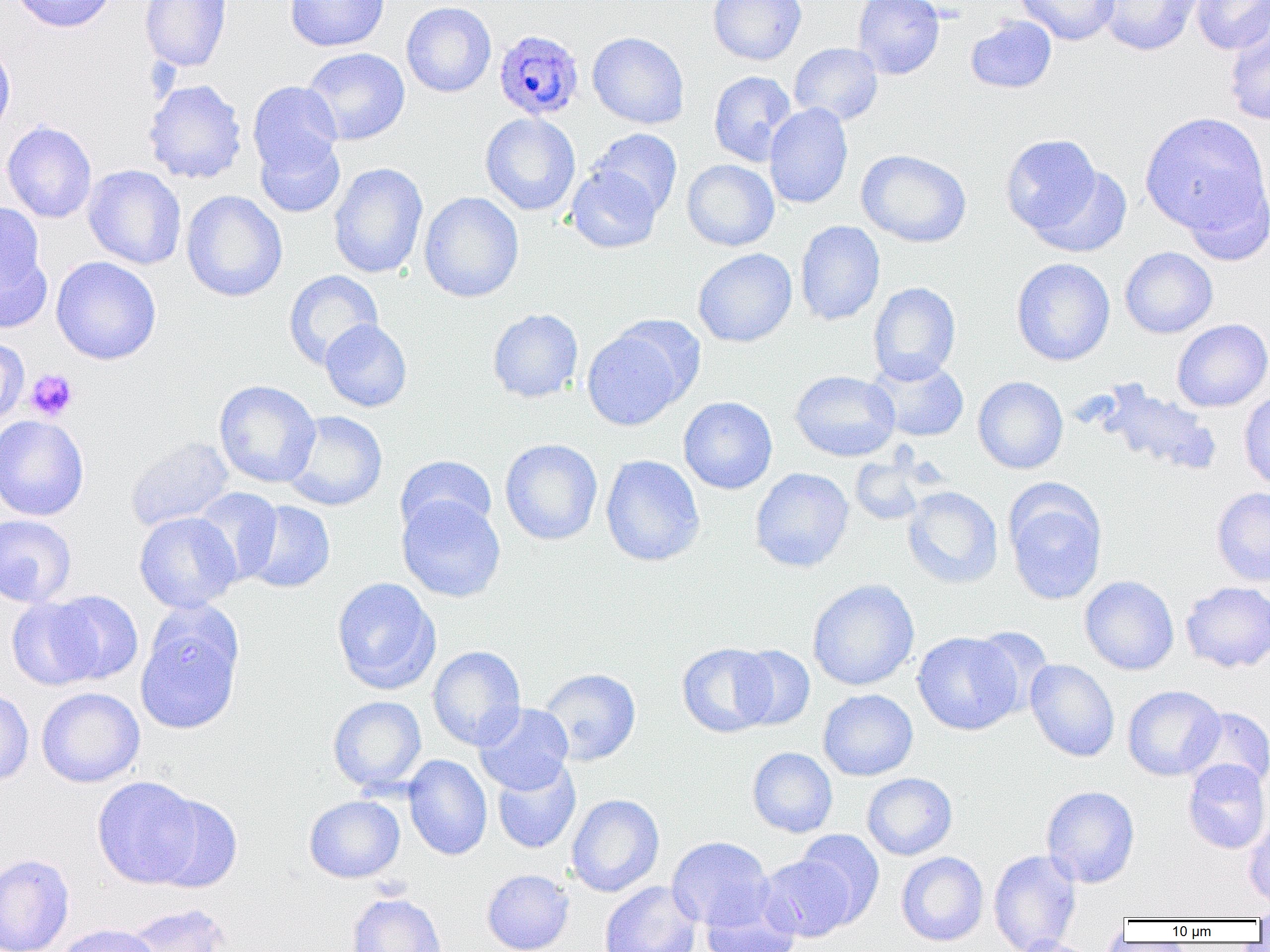
Summary:
  - Coordinate format: approximate bounding boxes as (x1, y1, x2, y2) in pixels
  - Platelet locations: (25, 369, 78, 422)
  - Uninfected red blood cell locations: (9, 0, 117, 33), (140, 0, 232, 71), (284, 0, 390, 52), (707, 0, 807, 65), (852, 0, 945, 79), (1016, 0, 1121, 45), (1097, 0, 1204, 56), (1191, 0, 1269, 55), (401, 1, 497, 97), (966, 15, 1057, 94), (1223, 16, 1270, 126), (587, 32, 689, 129), (0, 37, 15, 142), (788, 42, 883, 126), (302, 47, 410, 145), (708, 70, 798, 166), (143, 79, 248, 184), (248, 81, 343, 175), (764, 103, 853, 209), (480, 112, 581, 216), (1140, 113, 1268, 235), (2, 121, 97, 223), (589, 128, 683, 217), (254, 133, 346, 218), (999, 134, 1107, 239), (856, 149, 972, 248), (682, 159, 779, 251), (328, 162, 428, 279), (1027, 163, 1133, 257), (83, 164, 186, 270), (566, 165, 662, 253), (1180, 170, 1269, 265), (181, 190, 287, 302), (419, 191, 524, 302), (0, 202, 51, 325), (795, 220, 885, 326), (1120, 247, 1218, 338), (693, 248, 797, 347), (1012, 254, 1217, 348), (50, 256, 162, 365), (1011, 257, 1115, 366), (283, 270, 383, 370), (868, 281, 961, 384), (487, 308, 584, 402), (320, 319, 412, 412), (1172, 319, 1270, 412), (581, 323, 696, 431), (0, 337, 29, 427), (867, 357, 969, 442), (789, 370, 900, 462), (972, 376, 1068, 474), (214, 380, 320, 488), (1091, 380, 1222, 477), (1239, 389, 1270, 492), (678, 396, 777, 494), (283, 410, 388, 511), (0, 415, 89, 521), (125, 436, 234, 532), (500, 438, 603, 545), (600, 454, 705, 566), (850, 454, 930, 526), (395, 455, 497, 539), (749, 467, 854, 572), (1005, 484, 1107, 605), (903, 486, 1003, 589), (191, 487, 283, 585), (1211, 487, 1270, 587), (397, 495, 506, 602), (242, 500, 335, 593), (134, 511, 241, 614), (0, 514, 77, 607), (1079, 575, 1179, 675), (331, 577, 440, 695), (808, 579, 919, 691), (1180, 581, 1270, 672), (45, 590, 143, 685), (7, 596, 103, 691), (136, 612, 242, 735), (969, 626, 1051, 717), (912, 631, 1022, 735), (677, 642, 777, 738), (988, 644, 1098, 737), (428, 645, 526, 750), (733, 645, 816, 730), (1024, 659, 1120, 762), (537, 667, 641, 766), (1122, 685, 1225, 781), (0, 687, 34, 787), (36, 687, 145, 788), (818, 689, 918, 781), (327, 695, 427, 793), (473, 703, 574, 794), (1184, 707, 1270, 792), (747, 747, 837, 838), (403, 754, 492, 861), (492, 758, 581, 854), (1182, 759, 1270, 854), (861, 772, 958, 860), (91, 776, 205, 888), (1041, 785, 1140, 888), (149, 793, 243, 894), (566, 794, 664, 897), (304, 795, 405, 883), (1244, 821, 1270, 908), (794, 830, 885, 927), (667, 836, 774, 930), (988, 849, 1082, 952), (896, 851, 989, 946), (0, 854, 75, 952), (758, 855, 856, 942), (482, 868, 574, 952), (599, 880, 701, 952), (347, 892, 446, 952), (700, 895, 800, 952), (1252, 901, 1270, 927), (122, 903, 232, 952), (52, 923, 162, 952), (1010, 936, 1100, 952)
  - Plasmodium ovale-infected red blood cell locations: (493, 28, 584, 121)
  - Slide-level diagnosis: Plasmodium ovale
  - Modality: optical microscopy
  - Field of view: one of a larger specimen
  - Preparation: thin blood film
  - Magnification: 1000x
  - Image size: 1270×952 pixels